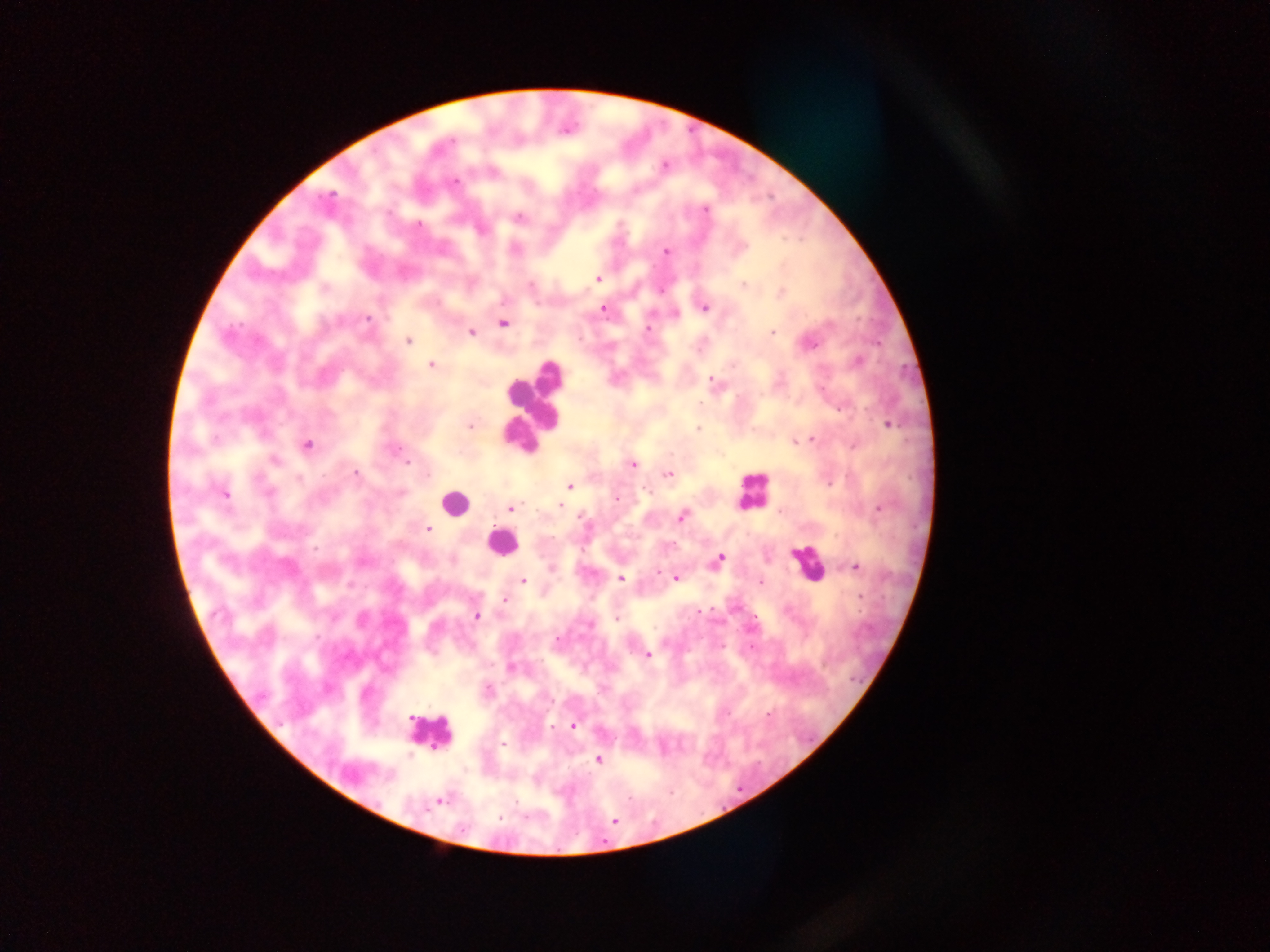
{
  "capture": "mobile-phone photograph through a microscope",
  "field_of_view": "single",
  "country": "Ghana",
  "leukocyte_locations": "approximate centers as {x, y} in pixels: {535, 403}, {751, 490}, {456, 502}, {501, 543}, {807, 564}, {429, 732}",
  "malaria_parasite_locations": "approximate centers as {x, y} in pixels: {664, 166}, {456, 182}, {330, 195}, {705, 209}, {519, 217}, {419, 224}, {665, 251}, {598, 278}, {743, 285}, {782, 292}, {704, 307}, {603, 309}, {367, 319}, {503, 324}, {830, 324}, {648, 329}, {471, 332}, {772, 333}, {408, 341}, {811, 345}, {859, 361}, {430, 365}, {733, 365}, {711, 379}, {699, 404}, {888, 425}, {470, 427}, {698, 429}, {812, 438}, {794, 442}, {307, 445}, {854, 446}, {275, 461}, {407, 462}, {632, 464}, {355, 474}, {668, 474}, {830, 482}, {570, 486}, {268, 492}, {225, 495}, {617, 499}, {559, 506}, {878, 508}, {511, 509}, {581, 517}, {681, 517}, {427, 529}, {316, 548}, {720, 557}, {856, 567}, {657, 572}, {677, 578}, {621, 579}, {523, 580}, {760, 581}, {860, 597}, {504, 600}, {699, 611}, {476, 616}, {617, 619}, {557, 640}, {648, 655}, {511, 668}, {487, 689}, {768, 713}, {573, 726}, {503, 744}, {410, 754}, {599, 759}, {439, 802}, {499, 817}, {614, 821}",
  "image_size": "1270×952 pixels",
  "preparation": "thick blood smear"
}